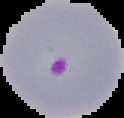
image type = segmented cell region with the area outside set to black
preparation = thin blood film
image size = 124×118 pixels
result = malaria parasites identified